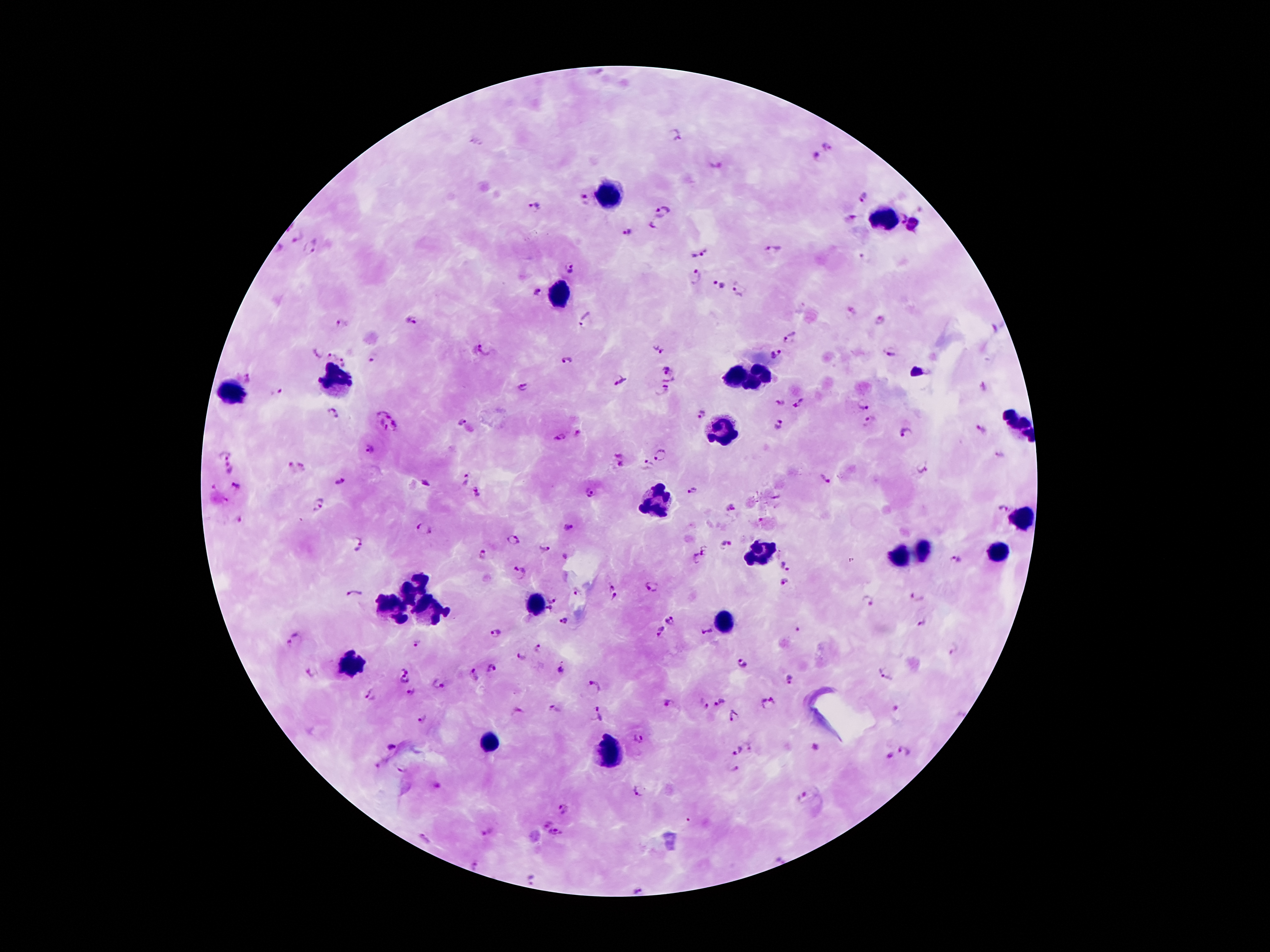
{
  "magnification": "100x",
  "capture": "smartphone through the microscope eyepiece",
  "plasmodium_parasite_locations": "approximate object centers, in pixels from the top-left corner: (x=678, y=135), (x=827, y=147), (x=817, y=156), (x=715, y=166), (x=864, y=197), (x=585, y=199), (x=535, y=206), (x=662, y=211), (x=849, y=218), (x=902, y=218), (x=914, y=228), (x=630, y=230), (x=296, y=237), (x=279, y=249), (x=313, y=250), (x=771, y=250), (x=700, y=251), (x=572, y=270), (x=694, y=279), (x=717, y=285), (x=538, y=291), (x=741, y=291), (x=881, y=319), (x=413, y=320), (x=584, y=320), (x=343, y=323), (x=790, y=338), (x=660, y=348), (x=484, y=350), (x=318, y=352), (x=890, y=352), (x=775, y=354), (x=332, y=356), (x=372, y=357), (x=343, y=362), (x=566, y=362), (x=667, y=370), (x=247, y=378), (x=620, y=379), (x=671, y=379), (x=525, y=386), (x=662, y=390), (x=276, y=392), (x=780, y=402), (x=800, y=403), (x=863, y=405), (x=383, y=412), (x=333, y=414), (x=702, y=414), (x=870, y=421), (x=461, y=422), (x=779, y=423), (x=395, y=426), (x=382, y=429), (x=982, y=429), (x=904, y=433), (x=559, y=437), (x=369, y=450), (x=225, y=452), (x=660, y=454), (x=999, y=455), (x=619, y=460), (x=647, y=465), (x=297, y=466), (x=922, y=467), (x=231, y=469), (x=463, y=480), (x=824, y=480), (x=341, y=481), (x=426, y=482), (x=236, y=485), (x=691, y=490), (x=476, y=493), (x=591, y=493), (x=777, y=498), (x=320, y=505), (x=731, y=508), (x=1003, y=509), (x=238, y=520), (x=568, y=528), (x=423, y=531), (x=514, y=540), (x=359, y=544), (x=726, y=544), (x=544, y=548), (x=699, y=554), (x=483, y=556), (x=564, y=557), (x=956, y=560), (x=784, y=568), (x=521, y=572), (x=786, y=581), (x=652, y=586), (x=611, y=588), (x=576, y=592), (x=355, y=595), (x=916, y=596), (x=615, y=597), (x=553, y=598), (x=866, y=601), (x=549, y=610), (x=671, y=619), (x=563, y=621), (x=923, y=622), (x=661, y=631), (x=707, y=632), (x=495, y=634), (x=294, y=639), (x=415, y=643), (x=539, y=649), (x=521, y=656), (x=742, y=665), (x=491, y=669), (x=405, y=670), (x=561, y=670), (x=312, y=671), (x=885, y=671), (x=474, y=675), (x=404, y=680), (x=789, y=680), (x=440, y=685), (x=596, y=685), (x=411, y=691), (x=370, y=696), (x=721, y=702), (x=769, y=702), (x=669, y=704), (x=704, y=704), (x=555, y=709), (x=520, y=711), (x=596, y=714), (x=735, y=716), (x=422, y=719), (x=639, y=739), (x=751, y=745), (x=814, y=746), (x=391, y=747), (x=903, y=749), (x=737, y=750), (x=890, y=756), (x=736, y=768), (x=437, y=786), (x=638, y=791), (x=803, y=797), (x=565, y=810), (x=546, y=824), (x=488, y=831), (x=556, y=835), (x=425, y=838), (x=475, y=867), (x=532, y=880), (x=639, y=889)",
  "field_of_view": "single",
  "leukocyte_locations": "approximate object centers, in pixels from the top-left corner: (x=609, y=192), (x=890, y=221), (x=560, y=296), (x=733, y=376), (x=757, y=379), (x=336, y=380), (x=232, y=391), (x=1021, y=425), (x=720, y=435), (x=655, y=501), (x=1025, y=514), (x=921, y=550), (x=757, y=552), (x=995, y=554), (x=898, y=556), (x=416, y=585), (x=535, y=604), (x=426, y=608), (x=392, y=610), (x=723, y=621), (x=353, y=667), (x=493, y=739), (x=607, y=755)",
  "preparation": "thick blood film",
  "stain": "Giemsa",
  "image_size": "1270×952 pixels",
  "patient_malaria_status": "positive for Plasmodium falciparum"
}